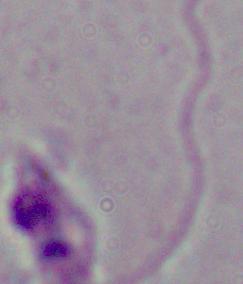 A Leishmania parasite is shown. 1000x magnification. Micrograph.